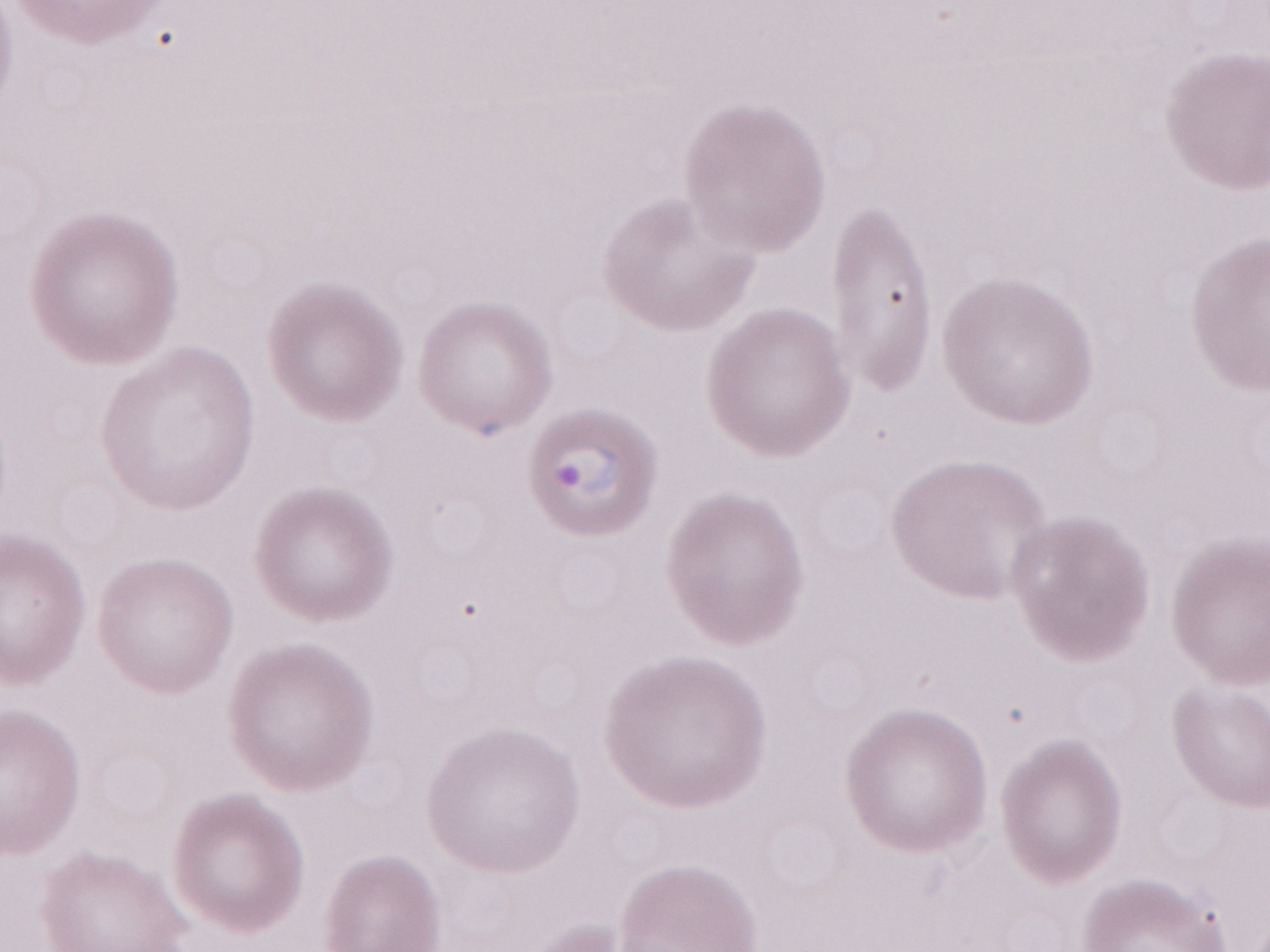
May-Grünwald-Giemsa stain. Single field of view. Patient diagnosis: malaria infection. Magnification: 1,000x. Thin peripheral-blood smear. Olympus BX43 microscope and DP73 digital camera. Image is 1270×952 pixels.